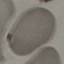
Summary:
  - Malaria status: uninfected
  - Stain: Giemsa
  - Capture: smartphone through the microscope eyepiece
  - Image type: cell patch, automatically extracted from a larger field of view and resized to 64 × 64 pixels
  - Preparation: thin smear